Locate and identify every blood parasite.
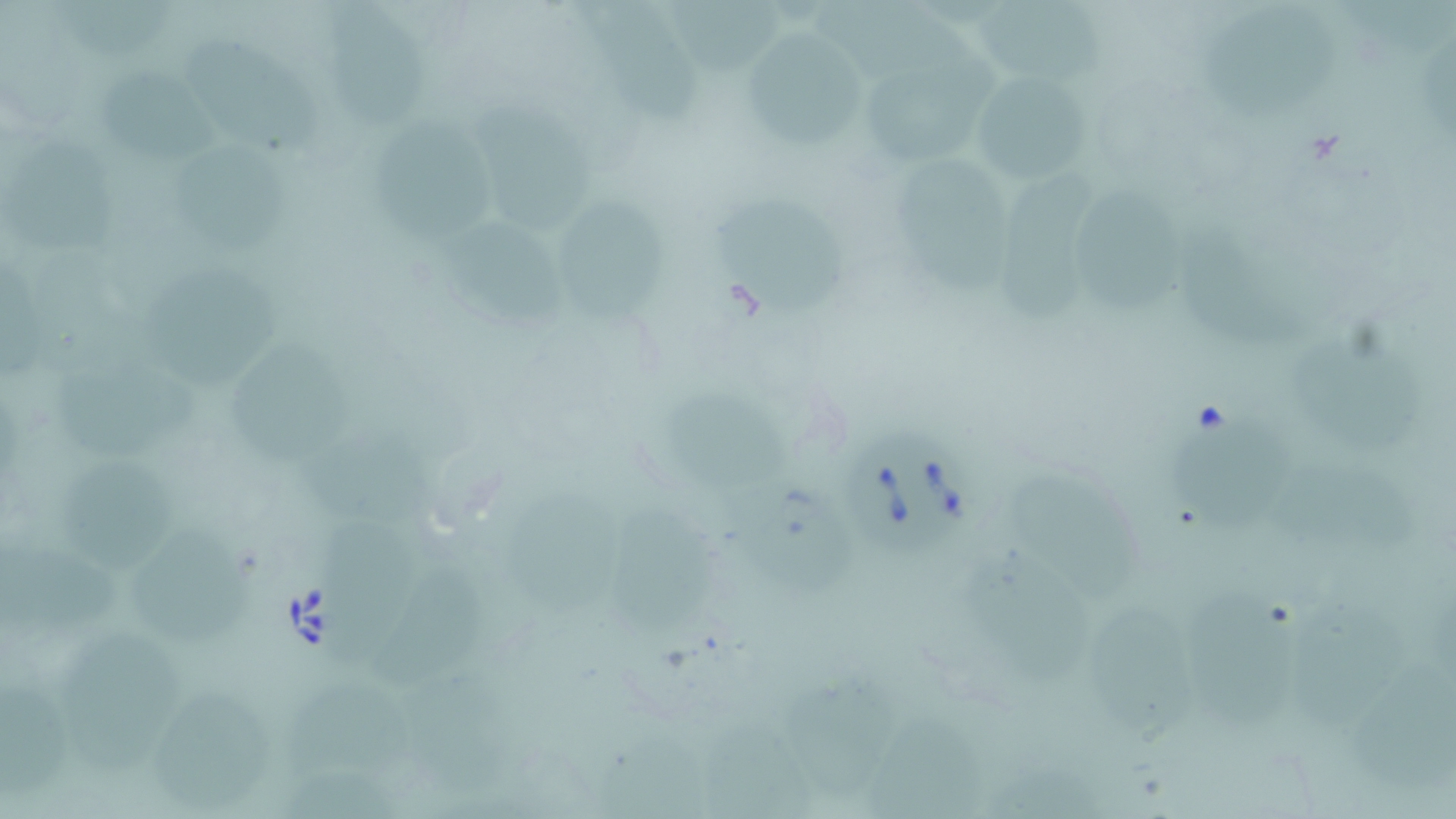
Approximate bounding boxes as named x1/y1/x2/y2 corners in pixels.
Babesia divergens-infected red blood cells: (x1=838, y1=422, x2=976, y2=558).
No Plasmodium falciparum, Plasmodium ovale, Plasmodium malariae, Plasmodium vivax, or Trypanosoma brucei observed.

{
  "slide_level_diagnosis": "Babesia divergens",
  "stain": "May-Grünwald-Giemsa",
  "magnification": "1000x",
  "field_of_view": "single",
  "uninfected_red_blood_cell_locations": "approximate bounding boxes as named x1/y1/x2/y2 corners in pixels: (x1=46, y1=1, x2=175, y2=62), (x1=320, y1=1, x2=435, y2=134), (x1=669, y1=1, x2=790, y2=73), (x1=970, y1=2, x2=1110, y2=81), (x1=590, y1=3, x2=704, y2=125), (x1=815, y1=4, x2=1002, y2=110), (x1=1197, y1=12, x2=1337, y2=120), (x1=182, y1=32, x2=320, y2=157), (x1=741, y1=34, x2=873, y2=150), (x1=863, y1=64, x2=983, y2=167), (x1=93, y1=67, x2=220, y2=165), (x1=971, y1=67, x2=1095, y2=191), (x1=473, y1=100, x2=590, y2=235), (x1=374, y1=116, x2=490, y2=262), (x1=4, y1=136, x2=122, y2=260), (x1=178, y1=139, x2=292, y2=255), (x1=892, y1=150, x2=1015, y2=307), (x1=990, y1=165, x2=1103, y2=323), (x1=1070, y1=186, x2=1193, y2=313), (x1=555, y1=196, x2=664, y2=326), (x1=713, y1=198, x2=844, y2=317), (x1=446, y1=215, x2=578, y2=327), (x1=1189, y1=239, x2=1301, y2=355), (x1=139, y1=257, x2=286, y2=392), (x1=1283, y1=327, x2=1424, y2=460), (x1=226, y1=334, x2=358, y2=467), (x1=50, y1=349, x2=206, y2=461), (x1=670, y1=388, x2=788, y2=501), (x1=1163, y1=410, x2=1299, y2=536), (x1=304, y1=416, x2=455, y2=534), (x1=53, y1=454, x2=178, y2=573), (x1=1262, y1=460, x2=1420, y2=556), (x1=1004, y1=463, x2=1133, y2=602), (x1=495, y1=475, x2=632, y2=625), (x1=737, y1=477, x2=872, y2=603), (x1=612, y1=500, x2=724, y2=644), (x1=319, y1=521, x2=428, y2=672), (x1=125, y1=523, x2=255, y2=649), (x1=3, y1=536, x2=133, y2=652), (x1=966, y1=551, x2=1091, y2=684), (x1=369, y1=562, x2=485, y2=694), (x1=1187, y1=585, x2=1300, y2=738), (x1=1287, y1=592, x2=1412, y2=733), (x1=1089, y1=602, x2=1193, y2=747), (x1=58, y1=631, x2=189, y2=778), (x1=784, y1=677, x2=894, y2=799), (x1=0, y1=679, x2=73, y2=800), (x1=286, y1=681, x2=412, y2=786), (x1=150, y1=691, x2=274, y2=810), (x1=867, y1=710, x2=986, y2=815)",
  "preparation": "thin blood smear",
  "image_size": "1456×819 pixels",
  "modality": "light microscopy"
}